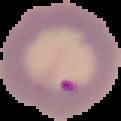
Summary:
  - Preparation: thin blood film
  - Image size: 121×121 pixels
  - Image type: segmented cell region with the area outside set to black
  - Malaria status: parasitized